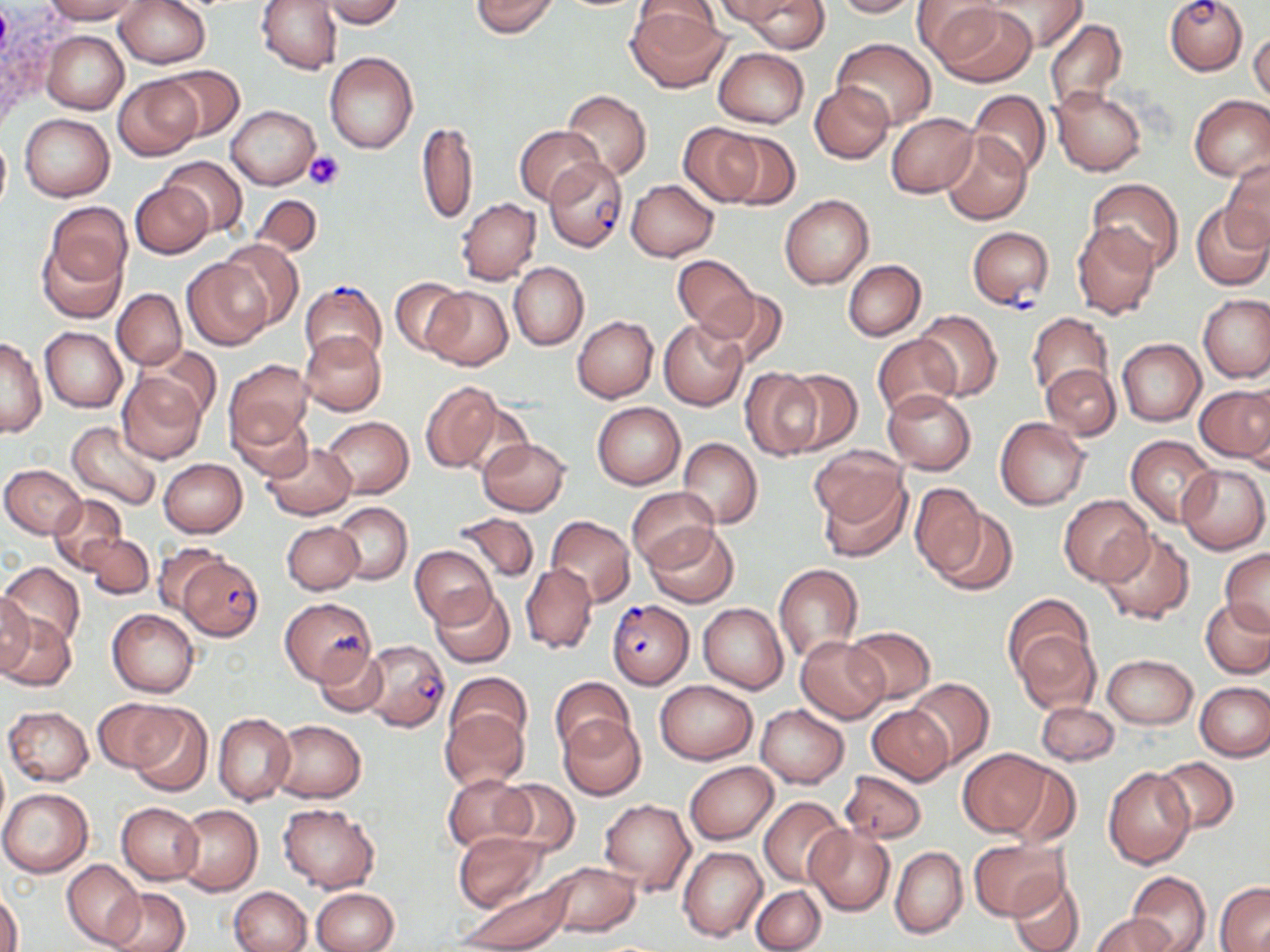

Approximate bounding boxes as (x1,y1)-(x2,y2) corner pairs in pixels. Uninfected red blood cell locations: (42,0)-(141,23), (256,0)-(341,73), (321,0)-(405,28), (470,0)-(560,37), (714,0)-(801,27), (742,0)-(827,52), (833,0)-(923,17), (980,0)-(1087,51), (116,1)-(209,69), (913,1)-(1003,64), (627,3)-(727,92), (931,4)-(1038,87), (1044,19)-(1127,112), (41,30)-(129,115), (1249,30)-(1270,105), (832,39)-(936,129), (713,48)-(809,128), (324,51)-(419,154), (160,66)-(244,141), (114,76)-(201,160), (809,82)-(894,164), (1049,87)-(1146,176), (562,89)-(652,181), (968,89)-(1052,178), (1189,94)-(1270,180), (227,106)-(319,189), (21,112)-(114,200), (885,113)-(977,198), (416,122)-(478,227), (677,122)-(765,207), (515,125)-(603,205), (715,125)-(801,208), (0,133)-(11,214), (941,133)-(1032,225), (161,157)-(247,235), (1221,157)-(1269,248), (1087,178)-(1184,272), (627,179)-(718,261), (130,180)-(212,258), (250,194)-(323,257), (780,195)-(873,288), (456,198)-(541,286), (44,202)-(132,288), (1191,202)-(1270,291), (1072,220)-(1160,319), (38,237)-(125,323), (217,240)-(303,331), (673,255)-(758,335), (182,260)-(269,350), (843,260)-(925,340), (509,262)-(588,350), (389,277)-(470,358), (423,287)-(513,370), (703,288)-(789,367), (112,289)-(186,369), (1197,295)-(1270,383), (914,311)-(1003,400), (1026,312)-(1112,398), (572,315)-(658,402), (657,317)-(748,411), (40,327)-(127,413), (300,331)-(387,416), (872,335)-(961,419), (0,338)-(45,438), (1117,338)-(1205,425), (142,345)-(222,423), (223,359)-(313,456), (1041,364)-(1120,440), (739,367)-(822,460), (779,370)-(862,453), (117,371)-(207,464), (421,380)-(504,475), (1195,384)-(1270,467), (882,388)-(976,474), (591,402)-(685,490), (228,404)-(313,484), (322,417)-(413,499), (995,419)-(1092,509), (66,421)-(164,512), (1125,435)-(1219,526), (478,437)-(570,515), (678,437)-(762,527), (263,441)-(357,519), (809,448)-(906,526), (159,458)-(247,537), (1177,463)-(1269,554), (1,464)-(86,538), (816,471)-(913,563), (909,482)-(986,578), (628,486)-(718,571), (50,495)-(127,573), (1058,496)-(1154,586), (332,502)-(413,585), (928,503)-(1019,595), (452,512)-(539,584), (545,515)-(635,605), (281,521)-(363,595), (645,524)-(741,609), (1097,529)-(1197,627), (82,535)-(154,600), (151,542)-(227,614), (409,544)-(496,629), (1220,549)-(1270,634), (2,562)-(85,650), (520,563)-(598,654), (773,563)-(864,663), (431,587)-(517,668), (0,590)-(34,677), (1003,595)-(1095,683), (280,597)-(375,685), (1201,599)-(1270,678), (698,602)-(788,693), (108,609)-(200,698), (0,614)-(76,691), (846,625)-(936,704), (1011,625)-(1100,713), (796,635)-(889,723), (313,646)-(388,719), (1103,654)-(1198,728), (444,672)-(532,750), (549,677)-(635,758), (906,678)-(995,768), (654,680)-(758,764), (1195,681)-(1270,761), (94,698)-(174,771), (1034,701)-(1119,766), (125,704)-(213,796), (755,704)-(848,788), (868,704)-(954,785), (3,706)-(94,786), (440,708)-(529,790), (212,712)-(295,806), (558,715)-(645,802), (271,720)-(366,803), (958,750)-(1054,837), (1154,757)-(1239,835), (1000,761)-(1081,848), (685,762)-(778,843), (1104,767)-(1196,869), (840,769)-(927,844), (443,773)-(533,854), (493,779)-(580,858), (0,787)-(95,877), (758,796)-(847,887), (598,799)-(694,897), (117,802)-(203,885), (279,803)-(379,893), (173,805)-(262,896), (806,824)-(895,916), (454,831)-(549,913), (969,841)-(1067,921), (678,846)-(767,941), (890,846)-(967,939), (61,860)-(144,949), (545,861)-(641,939), (1126,871)-(1211,952), (1008,876)-(1084,952), (458,878)-(575,951), (1215,882)-(1270,952), (230,885)-(312,952), (751,885)-(826,952), (102,886)-(189,952), (311,888)-(399,952), (1,889)-(23,952), (1091,913)-(1177,952). Platelet locations: (304,150)-(344,191). Plasmodium falciparum-infected red blood cell locations: (1165,0)-(1248,75), (543,157)-(628,251), (968,227)-(1053,308), (299,280)-(387,367), (178,553)-(264,642), (607,598)-(694,689), (361,640)-(450,732). Slide-level diagnosis: Plasmodium falciparum. Optical microscopy. Thin blood film. Single field of view. 1000x magnification. Image is 1270×952 pixels. May-Grünwald-Giemsa stain.